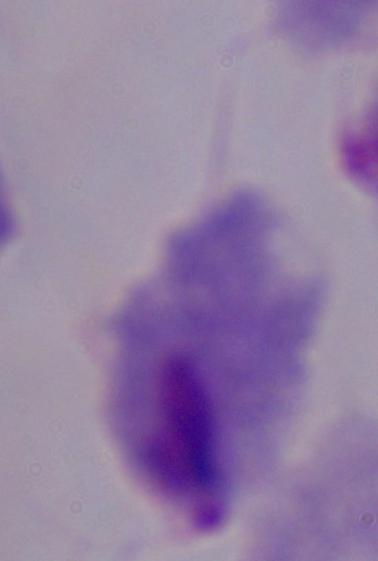

Summary:
  - Modality: photomicrograph
  - Magnification: 1000x
  - Identification: trichomonad